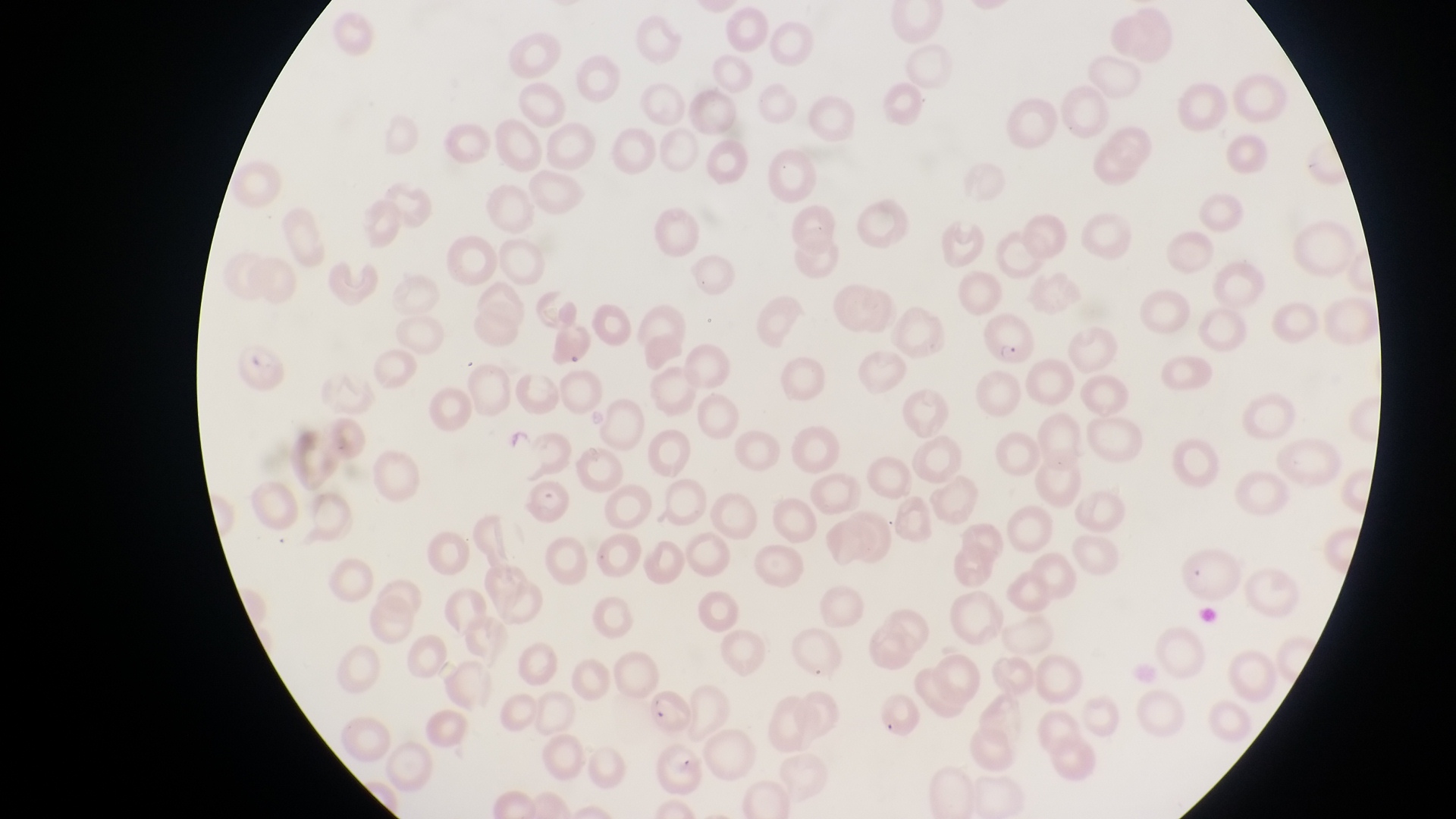
image_size: 1456×819 pixels
capture: smartphone photograph through the eyepiece of an Olympus CX-23 microscope
parasitised_red_blood_cell_locations: 'approximate bounding boxes as {left, top, right, bottom} in pixels: {981, 310, 1037, 369}, {234, 344, 292, 400}, {519, 475, 569, 531}, {647, 689, 696, 736}'
preparation: thin blood smear
magnification: 1000x
field_of_view: single
country: Uganda